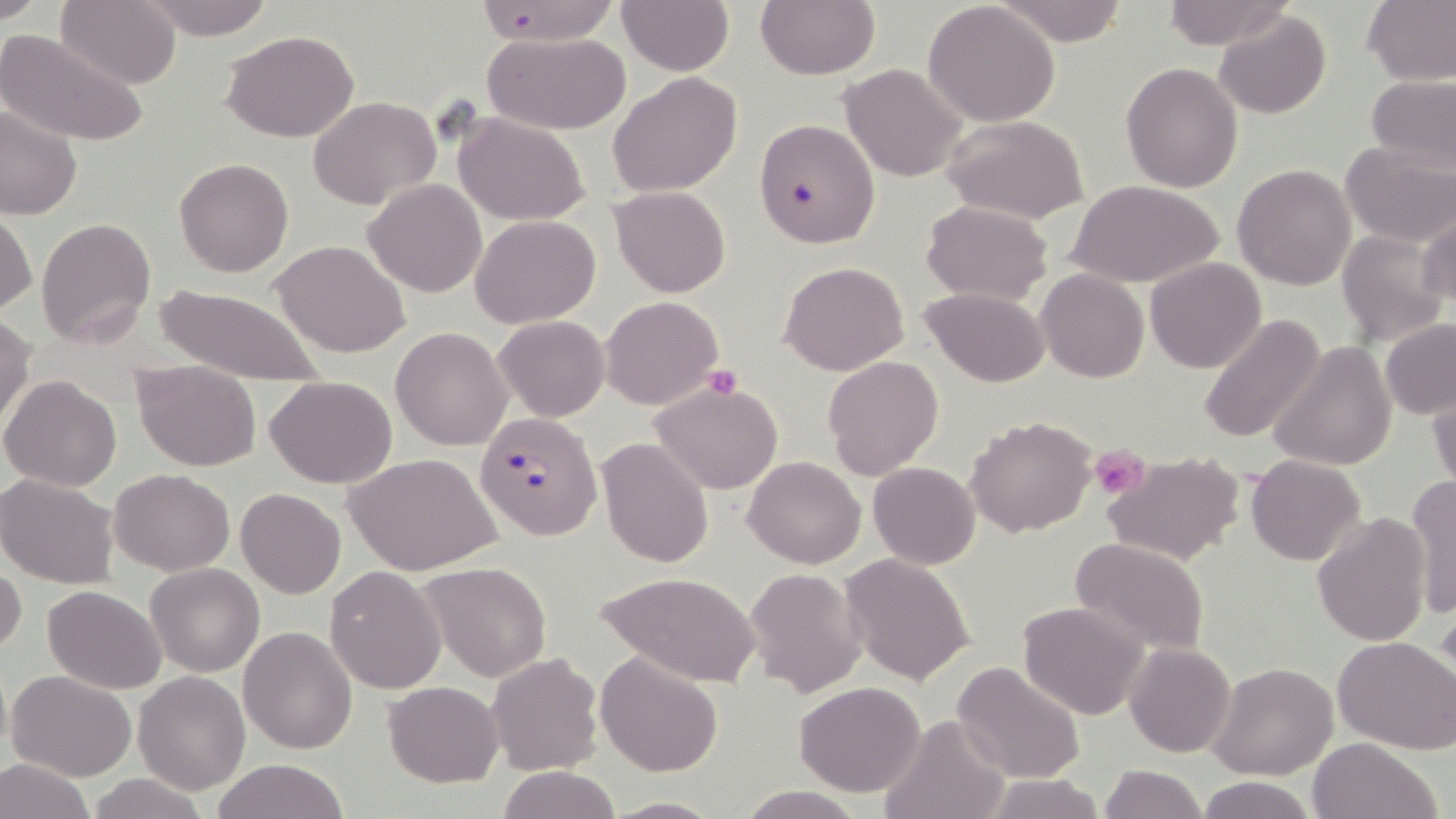
Summary:
  - Coordinate format: approximate bounding boxes as (x1,y1)-(x2,y2) corner pairs in pixels
  - Uninfected red blood cell locations: (57,0)-(182,89), (134,0)-(276,40), (617,0)-(734,74), (755,0)-(879,80), (994,0)-(1133,46), (1160,0)-(1292,50), (1361,0)-(1456,86), (922,2)-(1062,129), (1214,11)-(1332,120), (0,27)-(148,148), (221,29)-(361,143), (483,32)-(631,133), (1120,62)-(1242,193), (837,63)-(967,181), (608,71)-(743,197), (1365,74)-(1456,176), (307,95)-(441,209), (0,104)-(82,221), (452,112)-(591,224), (941,114)-(1090,225), (1339,143)-(1455,248), (174,158)-(293,277), (1232,164)-(1357,290), (363,179)-(487,298), (1070,179)-(1223,289), (609,185)-(731,298), (922,200)-(1052,305), (0,208)-(36,318), (1416,209)-(1456,315), (470,214)-(601,328), (36,218)-(157,349), (1337,228)-(1450,347), (271,239)-(410,357), (1145,257)-(1265,374), (778,260)-(909,375), (1036,269)-(1149,383), (148,283)-(329,390), (922,286)-(1050,387), (600,295)-(723,410), (0,312)-(36,432), (1197,314)-(1328,446), (494,315)-(610,422), (1379,316)-(1456,420), (391,328)-(512,450), (1268,339)-(1397,472), (822,355)-(943,478), (132,357)-(261,472), (1,374)-(123,492), (266,374)-(398,488), (649,381)-(784,495), (1428,383)-(1456,497), (966,416)-(1096,537), (596,438)-(715,569), (1101,450)-(1246,568), (347,453)-(502,576), (1245,454)-(1367,566), (743,456)-(866,569), (867,461)-(980,568), (110,469)-(235,575), (0,474)-(120,588), (1405,476)-(1456,620), (236,487)-(346,598), (1313,513)-(1432,646), (1069,538)-(1209,656), (841,554)-(976,686), (0,560)-(25,660), (146,562)-(265,677), (419,563)-(551,682), (325,565)-(446,694), (742,566)-(868,698), (594,571)-(762,687), (42,585)-(166,694), (1018,600)-(1148,720), (238,626)-(357,754), (1333,635)-(1455,753), (1124,642)-(1236,757), (595,650)-(723,777), (485,651)-(603,777), (951,660)-(1087,785), (1206,662)-(1339,781), (7,669)-(136,781), (133,671)-(251,793), (384,681)-(504,786), (794,681)-(925,796), (876,713)-(1015,819), (1305,738)-(1443,819), (0,756)-(94,819), (212,759)-(351,819), (1097,764)-(1207,819), (494,765)-(621,819), (981,774)-(1107,818), (84,775)-(212,819), (1193,775)-(1320,819), (735,785)-(870,818), (601,796)-(727,817)
  - Plasmodium falciparum-infected red blood cell locations: (468,0)-(625,48), (754,119)-(878,249), (474,412)-(601,541)
  - Platelet locations: (703,364)-(743,399), (1091,445)-(1150,498)
  - Slide-level diagnosis: Plasmodium falciparum
  - Modality: light microscopy
  - Stain: May-Grünwald-Giemsa
  - Preparation: thin blood smear
  - Field of view: one of a larger specimen
  - Image size: 1456×819 pixels
  - Magnification: 1000x